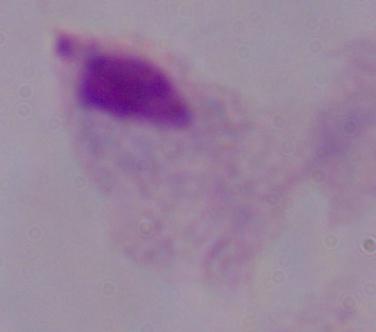

Micrograph. Captured at 1000x magnification. A trichomonad is shown.